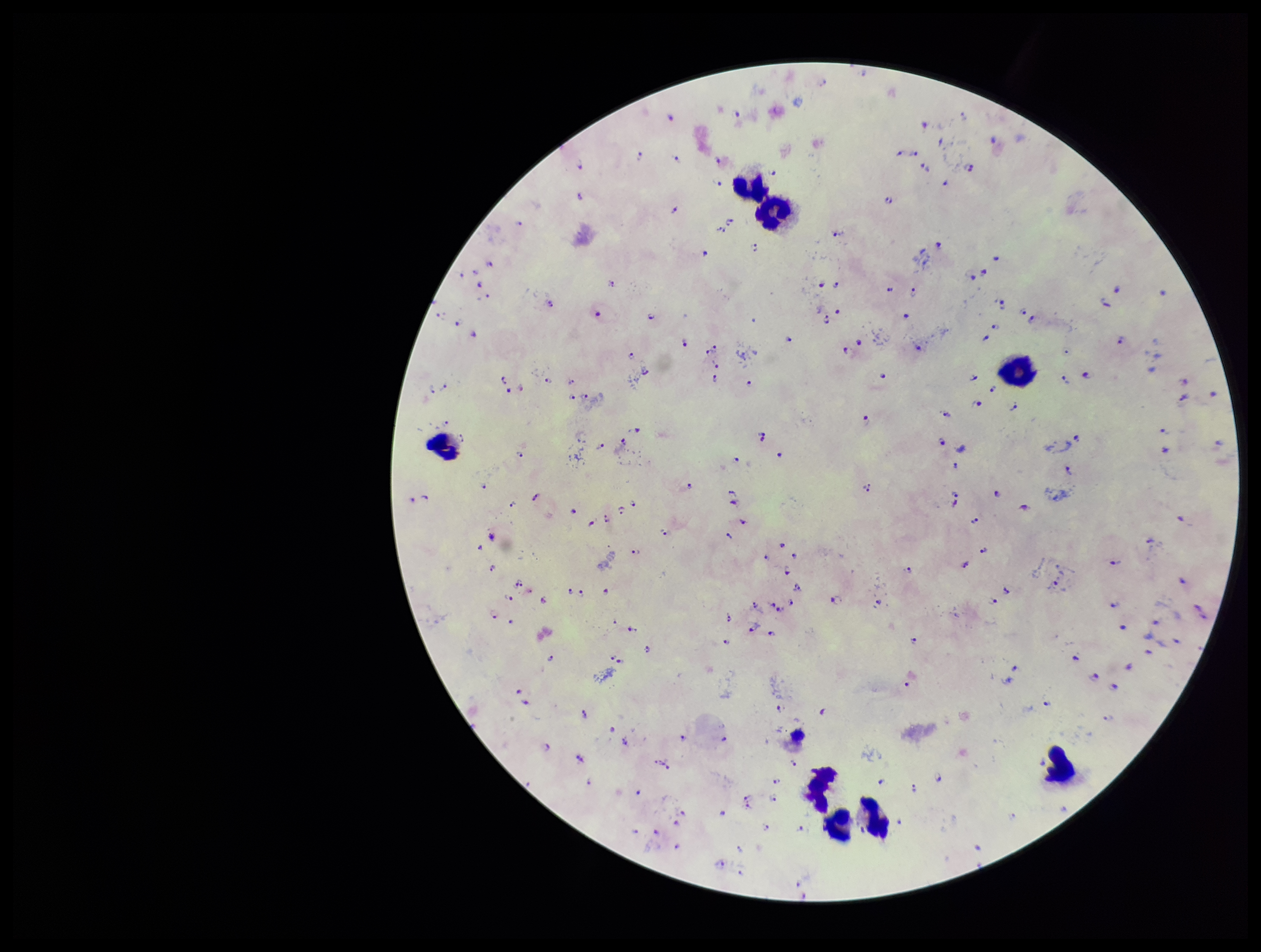
Summary:
  - Capture: smartphone photograph through the microscope eyepiece
  - Patient malaria status: infected
  - Parasite count: 174
  - Leukocyte count: 8
  - Plasmodium parasites: detected
  - Species reported for this patient: Plasmodium falciparum
  - Field of view: one from this slide
  - Image size: 1261×952 pixels
  - Preparation: thick
  - Stain: Giemsa